Assess this cell for malaria.
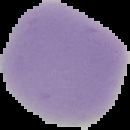
Uninfected.

Cell region segmented out of the field of view; the surrounding area is masked to black. Image is 130×130 pixels. From a thin blood smear.